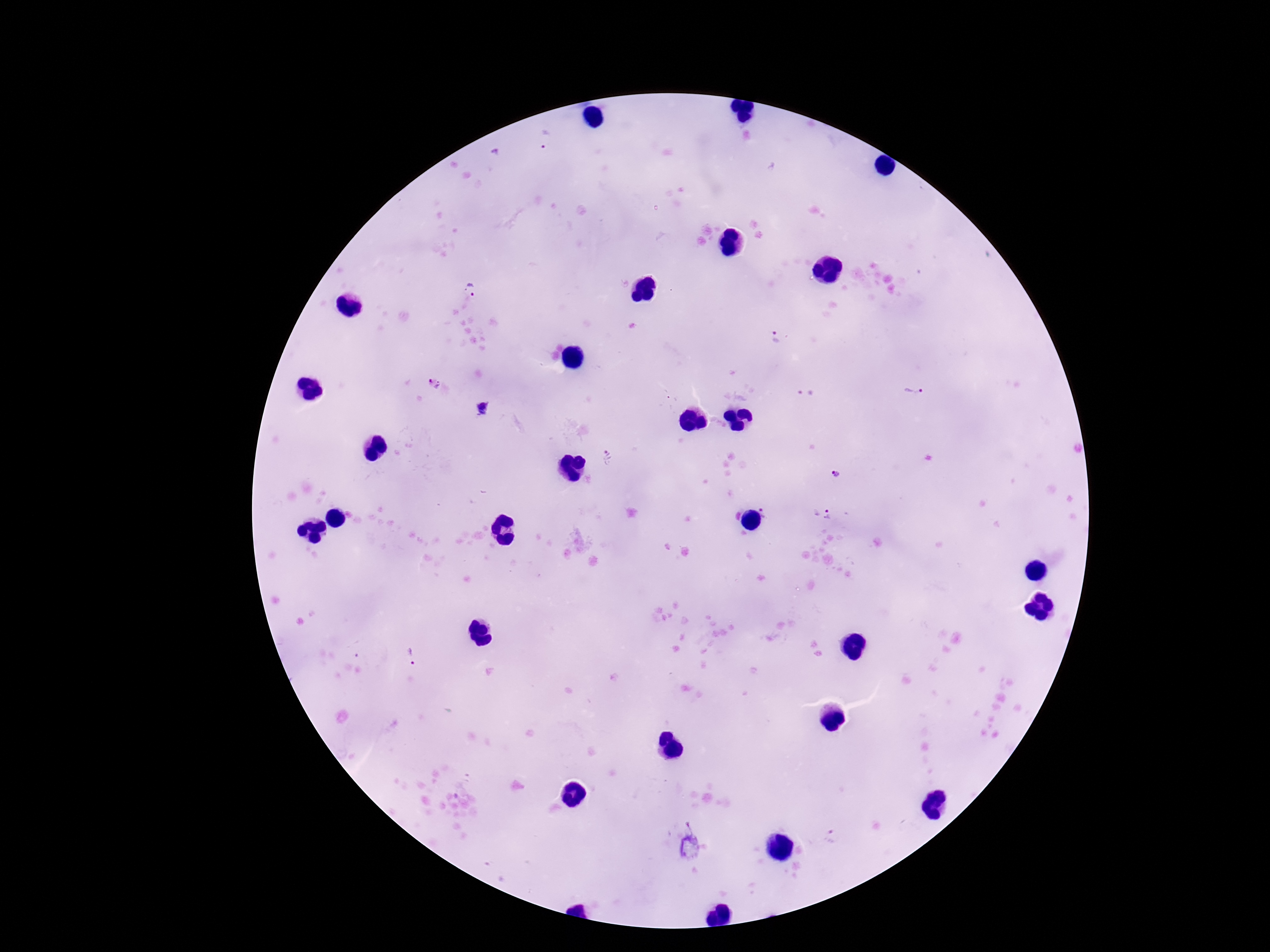 Approximate centers as {x, y} in pixels. Plasmodium parasite locations: {546, 141}, {468, 291}, {771, 338}, {435, 382}, {913, 388}, {805, 394}, {483, 409}, {608, 456}, {834, 476}, {768, 510}, {822, 514}, {411, 659}, {690, 847}. Photographed through the microscope eyepiece with a smartphone camera. Image is 1270×952 pixels. Single field of view. Giemsa stain. 100x magnification. Patient malaria status: positive. Thick peripheral-blood smear.